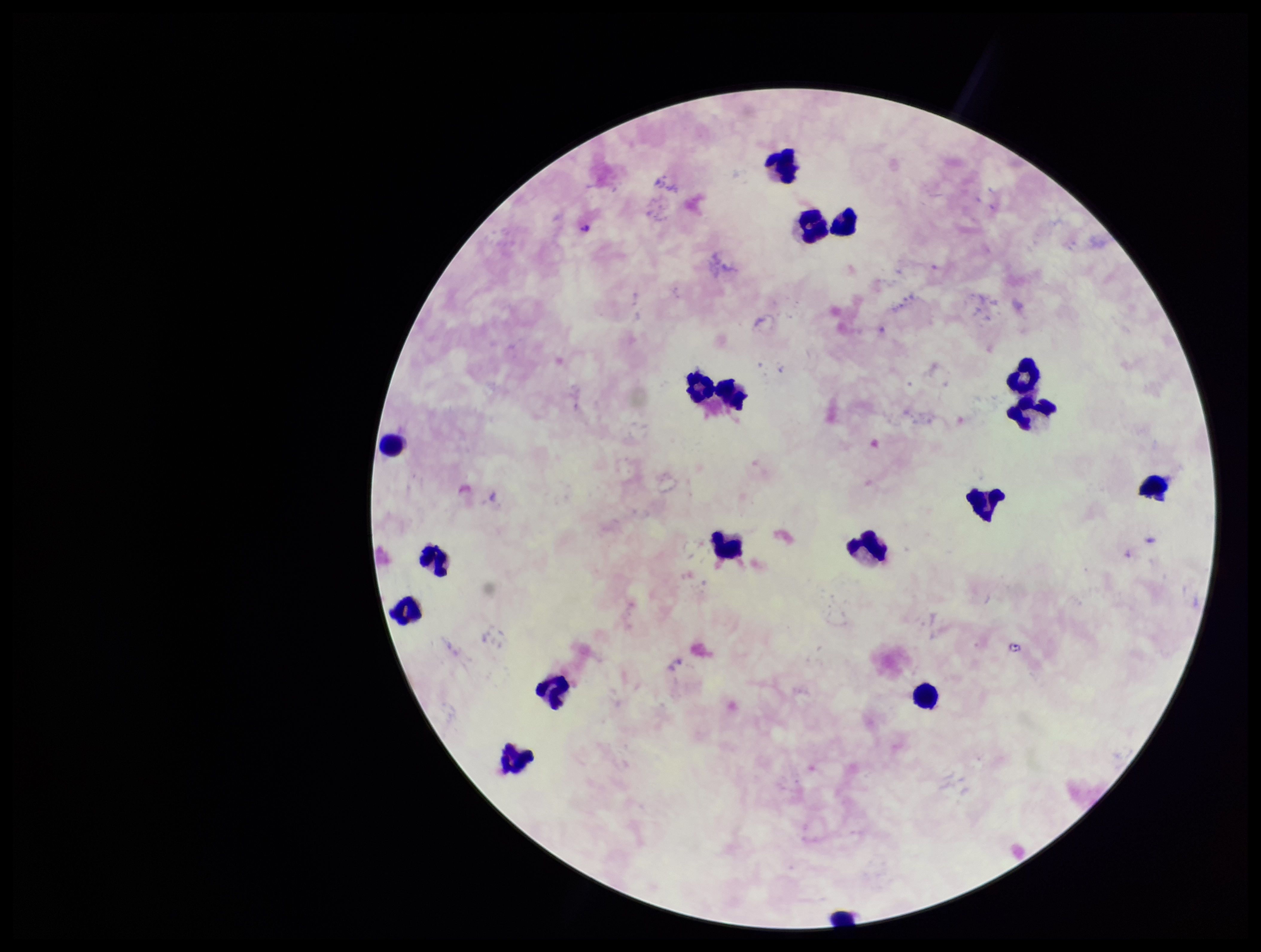

Parasite count: 0. One field from this slide. Leukocyte count: 17. Patient malaria status: negative. Stained with Giemsa. Image is 1261×952 pixels. Preparation: thick. Smartphone photograph taken through the eyepiece of a microscope. Plasmodium parasites: none detected.